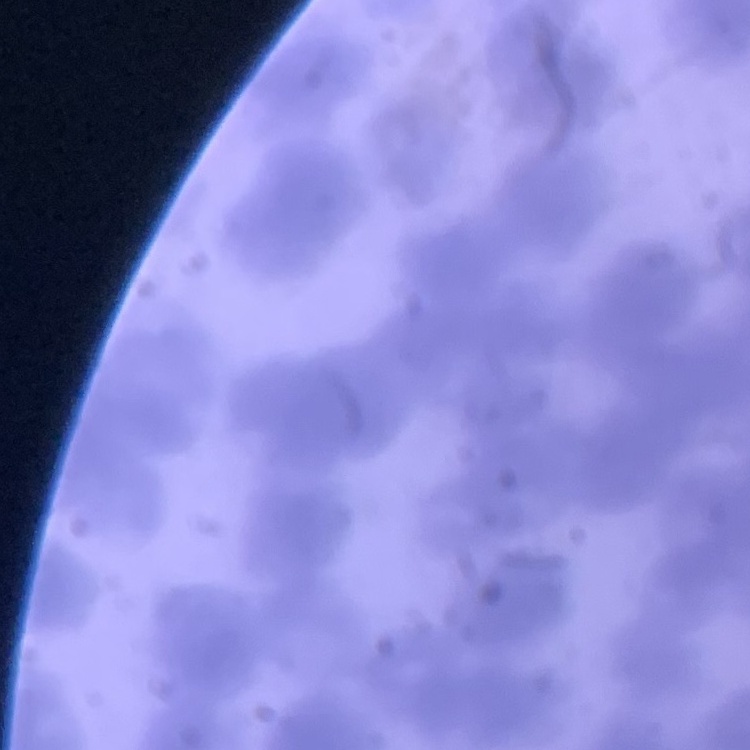
erythrocyte morphology = rouleaux formation
stain = Field's or Giemsa
preparation = thin blood film
image type = one tile cut from a larger photomicrograph